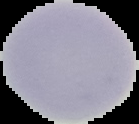
Summary:
  - Preparation: thin blood smear
  - Malaria status: uninfected
  - Image size: 139×124 pixels
  - Image type: cell region segmented out of the field of view; surrounding area masked to black